Locate every blood parasite and identify its species.
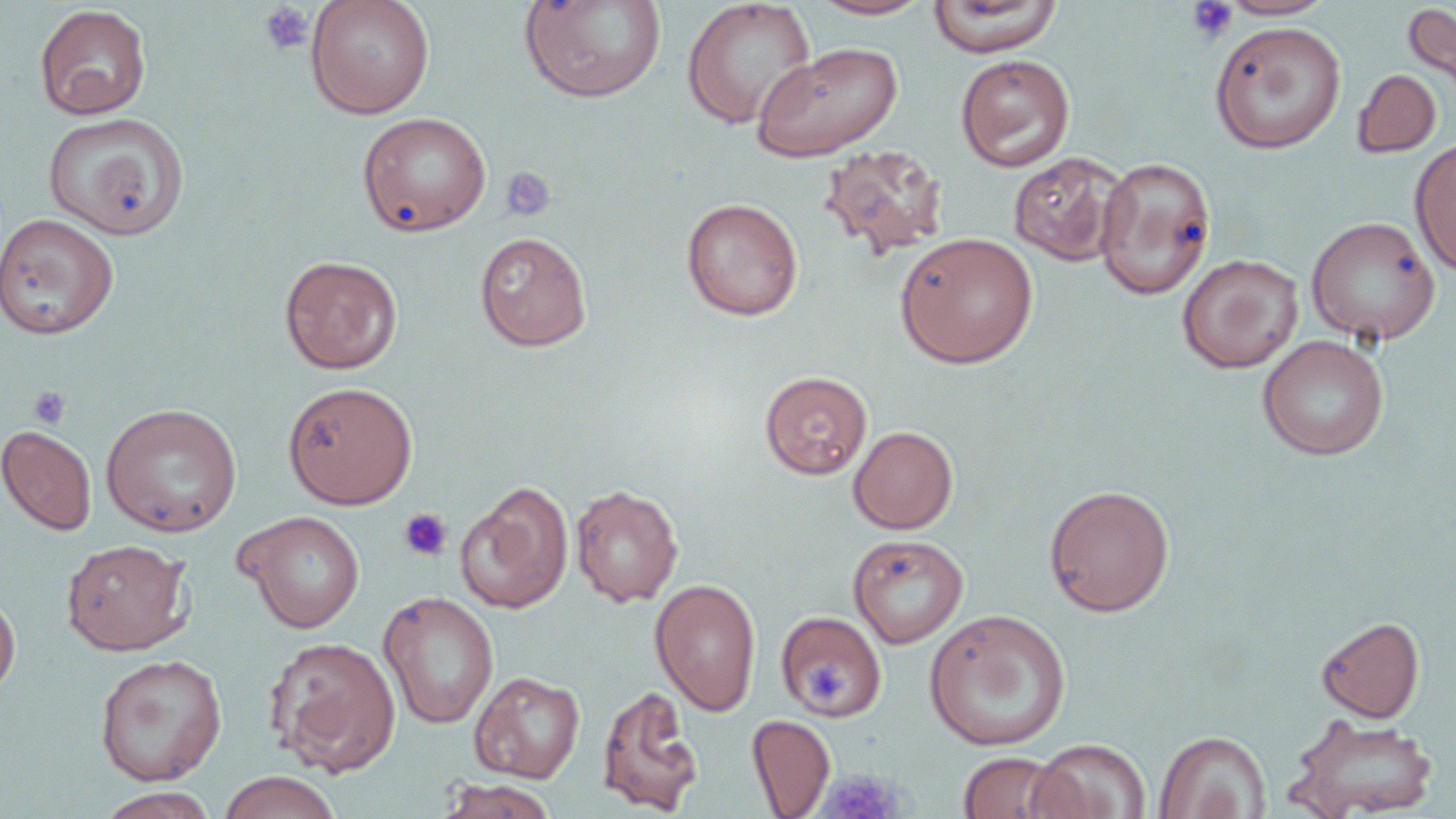
No blood parasites observed.

Summary:
  - Coordinate format: approximate bounding boxes as [x1, y1, x2, y2] in pixels
  - Uninfected red blood cell locations: [305, 0, 434, 119], [517, 0, 668, 104], [681, 0, 817, 129], [926, 0, 1061, 58], [1217, 0, 1336, 20], [806, 1, 937, 20], [1401, 3, 1456, 99], [34, 4, 151, 120], [1209, 20, 1346, 154], [752, 42, 903, 161], [955, 54, 1075, 172], [1352, 69, 1441, 158], [43, 112, 189, 241], [357, 112, 491, 235], [1409, 138, 1456, 276], [817, 143, 949, 263], [1008, 152, 1128, 266], [1094, 156, 1216, 300], [681, 198, 803, 321], [0, 213, 119, 340], [1306, 216, 1440, 345], [474, 231, 592, 351], [895, 232, 1039, 368], [1177, 254, 1303, 373], [279, 255, 403, 374], [1258, 335, 1389, 460], [759, 370, 872, 479], [282, 381, 418, 509], [100, 402, 242, 537], [0, 425, 97, 536], [849, 426, 958, 534], [456, 481, 574, 614], [570, 484, 683, 606], [1043, 484, 1175, 617], [236, 510, 365, 633], [847, 534, 969, 648], [61, 539, 193, 655], [649, 578, 761, 716], [0, 590, 20, 701], [378, 592, 500, 729], [924, 609, 1071, 751], [776, 611, 887, 721], [1316, 616, 1425, 723], [264, 635, 402, 776], [94, 654, 227, 786], [469, 671, 585, 783], [596, 684, 704, 816], [747, 714, 835, 818], [1286, 715, 1439, 819], [1154, 730, 1270, 819], [1027, 738, 1151, 819], [957, 751, 1070, 818], [217, 771, 342, 819], [437, 778, 558, 819], [94, 788, 223, 818]
  - Platelet locations: [1185, 1, 1238, 43], [259, 3, 315, 56], [501, 166, 558, 222], [29, 386, 71, 429], [398, 508, 453, 561], [803, 660, 853, 706], [820, 769, 902, 819]
  - Slide-level diagnosis: negative for blood parasites
  - Preparation: thin blood smear
  - Magnification: 1000x
  - Stain: May-Grünwald-Giemsa
  - Image size: 1456×819 pixels
  - Modality: optical microscopy
  - Field of view: one of a larger specimen